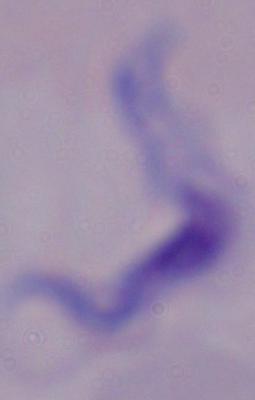

Summary:
  - Identification: trypanosome
  - Modality: photomicrograph
  - Magnification: 1000x